Point out Plasmodium parasites and leukocytes.
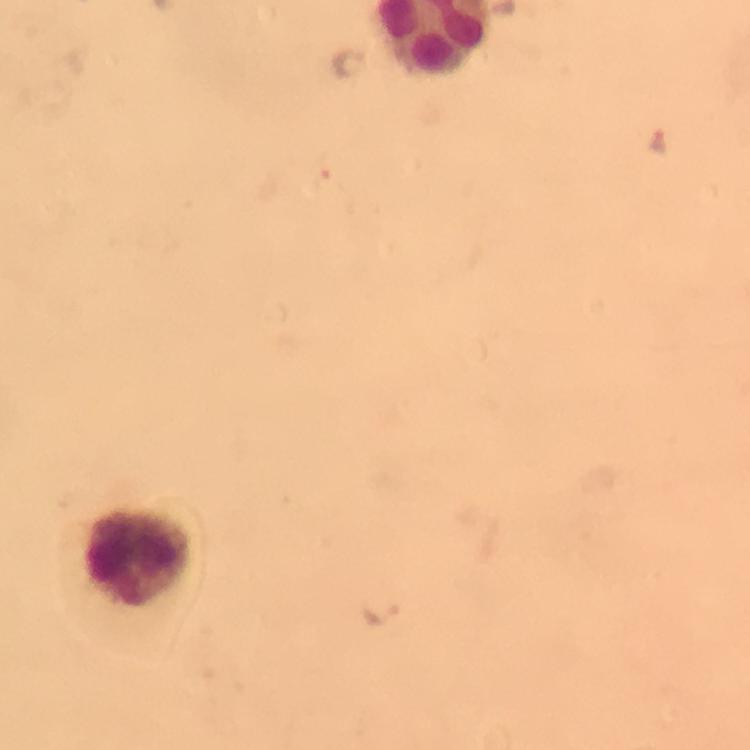
Approximate centers as (x, y) in pixels.
Plasmodium parasites: (349, 62), (658, 138), (380, 616).
Leukocytes: (150, 558).

magnification: 100x
preparation: thick smear
immersion_oil: used
context: from a diagnostic examination for malaria
image_size: 750×750 pixels
capture: smartphone photograph through a microscope
stain: Giemsa
cropped_from: one field of view